Classify this cell by malaria status.
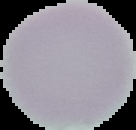

It is uninfected.

Image is 136×130 pixels. From a thin blood film. The area outside the segmented cell region is set to black.